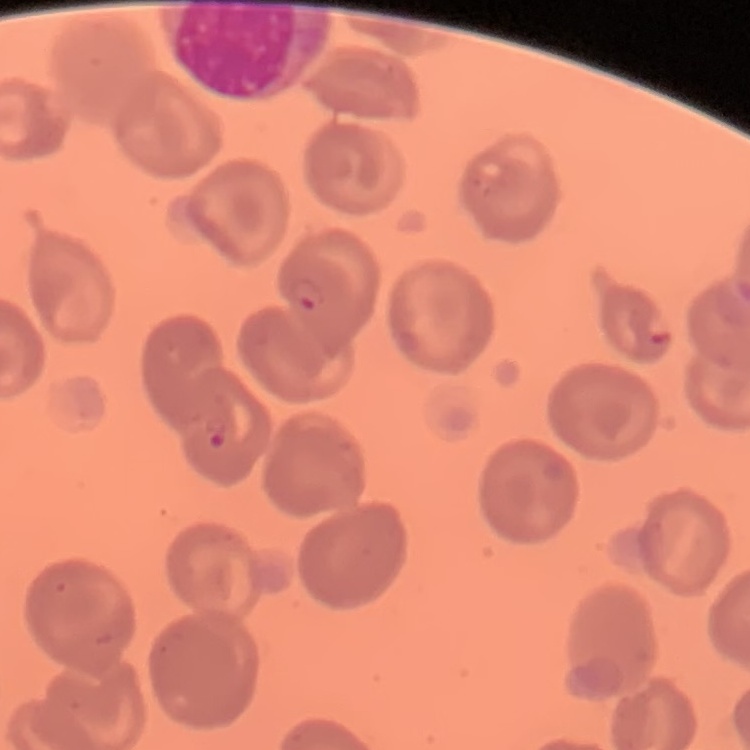
{
  "erythrocyte_morphology": "no rouleaux formation",
  "preparation": "thin peripheral smear",
  "image_type": "square crop of a larger photomicrograph",
  "stain": "Field's or Giemsa"
}